Classify this cell by malaria status.
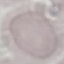

Uninfected.

image_type: automatically extracted cell patch, resized to 64 × 64 pixels
preparation: thin smear
capture: smartphone through the microscope eyepiece
stain: Giemsa